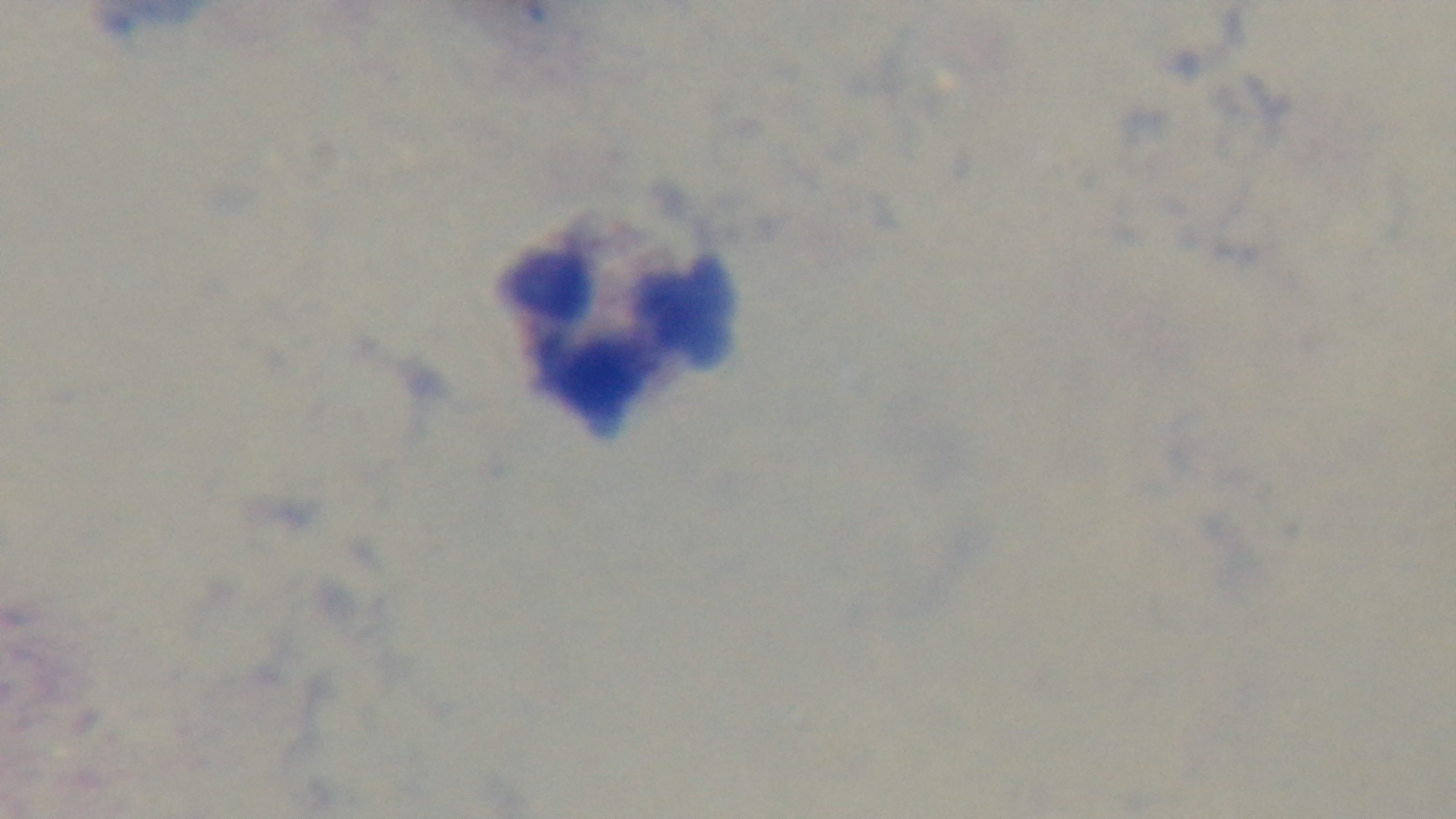

One field from the slide. Preparation: thick blood film. Giemsa-stained. Photomicrograph. Mounted 4K digital camera. Malaria status: negative. Oil-immersion objective, 100x.